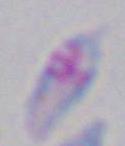 1000x magnification. Photomicrograph. Toxoplasma gondii is seen.